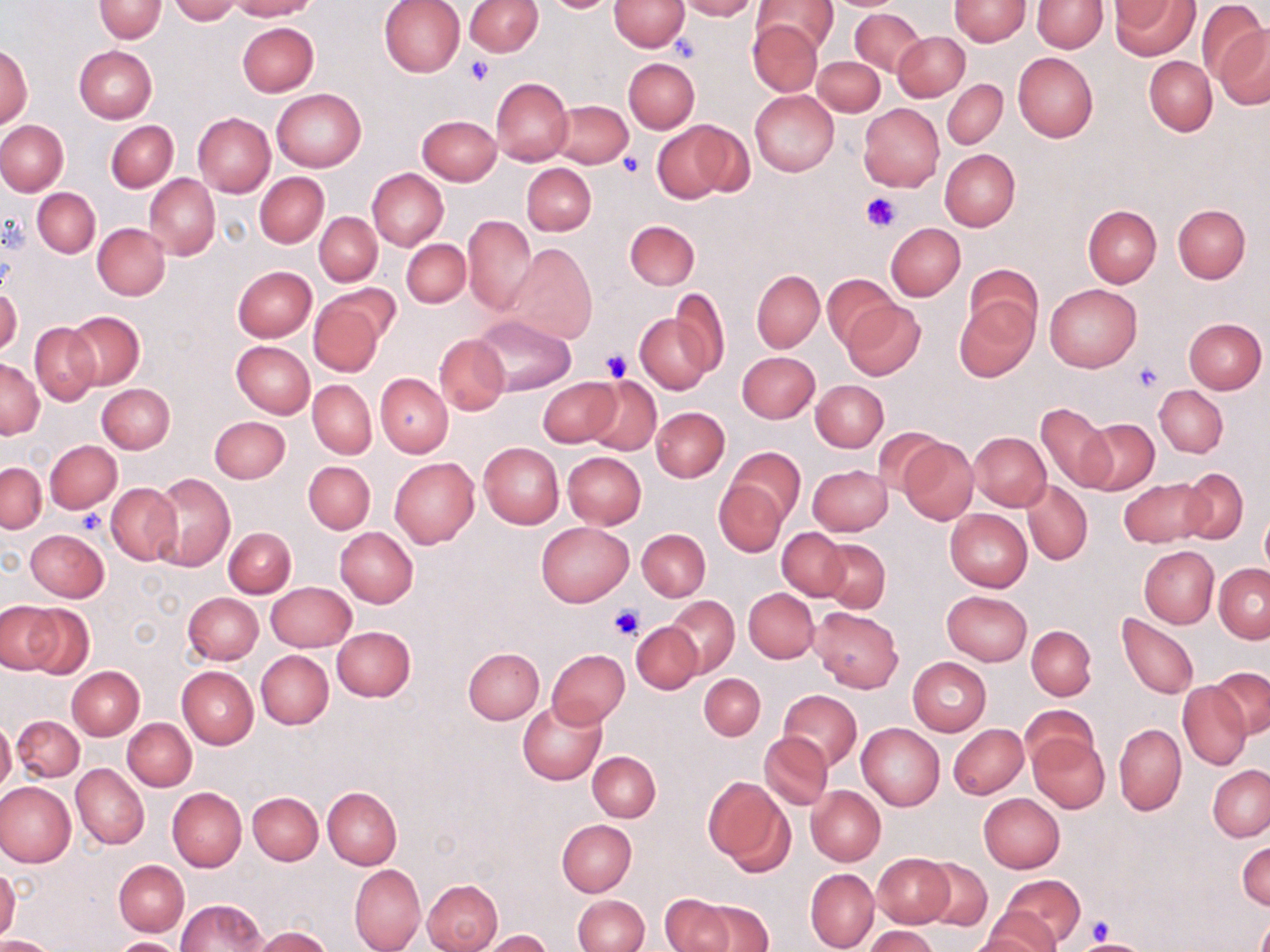
Approximate bounding boxes as (x1,y1)-(x2,y2) corner pairs in pixels. Platelet locations: (670,33)-(701,62), (464,56)-(494,85), (618,152)-(645,177), (860,191)-(902,233), (601,347)-(632,381), (1132,361)-(1163,391), (78,510)-(105,533), (609,606)-(644,640), (1085,916)-(1115,946). Uninfected red blood cell locations: (94,0)-(166,42), (231,0)-(317,20), (380,0)-(465,77), (609,0)-(688,51), (676,0)-(759,20), (948,0)-(1031,46), (1032,0)-(1107,52), (1110,0)-(1197,59), (169,1)-(240,23), (465,1)-(541,56), (751,1)-(836,54), (1196,1)-(1269,84), (850,8)-(926,76), (746,19)-(824,97), (237,21)-(319,97), (1215,26)-(1270,110), (894,32)-(969,102), (1,44)-(33,128), (73,46)-(156,123), (1011,52)-(1098,143), (624,56)-(699,133), (1145,56)-(1217,136), (813,57)-(884,115), (490,77)-(573,166), (943,79)-(1006,149), (272,88)-(365,172), (750,89)-(839,176), (551,99)-(632,168), (858,103)-(943,191), (192,113)-(275,198), (416,115)-(501,185), (0,120)-(68,195), (106,120)-(177,191), (653,120)-(753,202), (940,148)-(1020,231), (521,162)-(597,236), (367,169)-(448,250), (255,172)-(328,248), (144,173)-(220,260), (33,187)-(100,258), (1172,204)-(1251,283), (1083,205)-(1161,287), (315,212)-(382,285), (463,215)-(536,317), (625,220)-(699,289), (92,223)-(170,300), (885,223)-(965,301), (402,239)-(470,308), (504,243)-(597,345), (965,263)-(1040,337), (233,266)-(316,342), (752,270)-(824,351), (821,274)-(901,350), (1045,284)-(1141,373), (0,286)-(22,359), (668,287)-(730,378), (308,295)-(388,376), (841,299)-(926,381), (956,301)-(1037,381), (66,311)-(145,389), (635,311)-(714,394), (474,316)-(576,396), (1184,317)-(1267,393), (30,323)-(100,405), (434,334)-(509,415), (233,341)-(314,417), (737,351)-(819,423), (1,358)-(44,439), (376,373)-(453,456), (583,375)-(661,454), (537,377)-(620,446), (308,379)-(376,458), (812,380)-(888,452), (97,383)-(175,453), (1155,385)-(1227,457), (1036,403)-(1114,490), (652,407)-(729,482), (211,416)-(289,483), (1079,418)-(1159,495), (969,432)-(1051,511), (896,435)-(978,525), (44,440)-(121,512), (478,443)-(563,529), (727,446)-(805,523), (562,451)-(646,528), (389,457)-(479,548), (303,461)-(375,534), (1,462)-(44,533), (806,464)-(893,536), (1177,469)-(1248,544), (150,473)-(235,571), (1117,477)-(1209,547), (713,479)-(788,557), (1022,480)-(1093,565), (106,482)-(182,565), (945,508)-(1032,592), (1260,508)-(1270,578), (536,522)-(633,606), (224,527)-(295,598), (335,527)-(418,607), (776,528)-(850,601), (26,529)-(109,602), (637,529)-(709,601), (819,539)-(891,612), (1139,546)-(1218,628), (1214,563)-(1270,642), (266,581)-(355,652), (743,588)-(820,663), (942,590)-(1032,666), (183,592)-(264,664), (668,596)-(739,676), (12,602)-(93,679), (809,606)-(903,692), (1117,614)-(1199,701), (631,621)-(703,695), (1026,625)-(1095,699), (331,626)-(416,701), (463,647)-(543,724), (547,649)-(630,727), (256,650)-(333,729), (907,656)-(991,736), (177,665)-(259,748), (67,666)-(144,740), (1208,668)-(1270,738), (699,673)-(765,740), (1178,682)-(1251,771), (777,689)-(863,770), (517,699)-(606,784), (1020,704)-(1097,772), (12,716)-(84,782), (123,718)-(196,791), (0,720)-(15,795), (857,723)-(944,811), (1114,723)-(1186,815), (949,724)-(1027,798), (760,732)-(833,811), (1028,732)-(1108,813), (587,751)-(661,821), (71,763)-(149,850), (1208,765)-(1270,841), (703,777)-(794,873), (0,781)-(76,868), (323,786)-(401,869), (807,786)-(885,864), (168,787)-(247,872), (249,792)-(322,865), (978,792)-(1065,873), (557,819)-(637,896), (1237,839)-(1269,911), (873,853)-(954,928), (920,858)-(993,930), (115,860)-(189,936), (349,864)-(425,952), (0,866)-(21,942), (806,868)-(879,952), (998,873)-(1085,948), (422,879)-(503,952), (657,894)-(734,952), (574,895)-(648,952), (684,897)-(773,952), (176,899)-(267,952), (1256,911)-(1270,952), (979,915)-(1060,950), (865,926)-(938,952), (253,927)-(332,952), (481,930)-(552,952), (0,934)-(56,951), (110,937)-(188,952). Slide-level diagnosis: no evidence of blood parasites. Optical microscopy. Thin blood smear. May-Grünwald-Giemsa-stained preparation. Single field of view. 1000x magnification. Image is 1270×952 pixels.